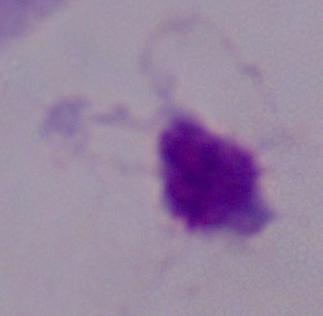

identification = trichomonad
magnification = 1000x
modality = photomicrograph